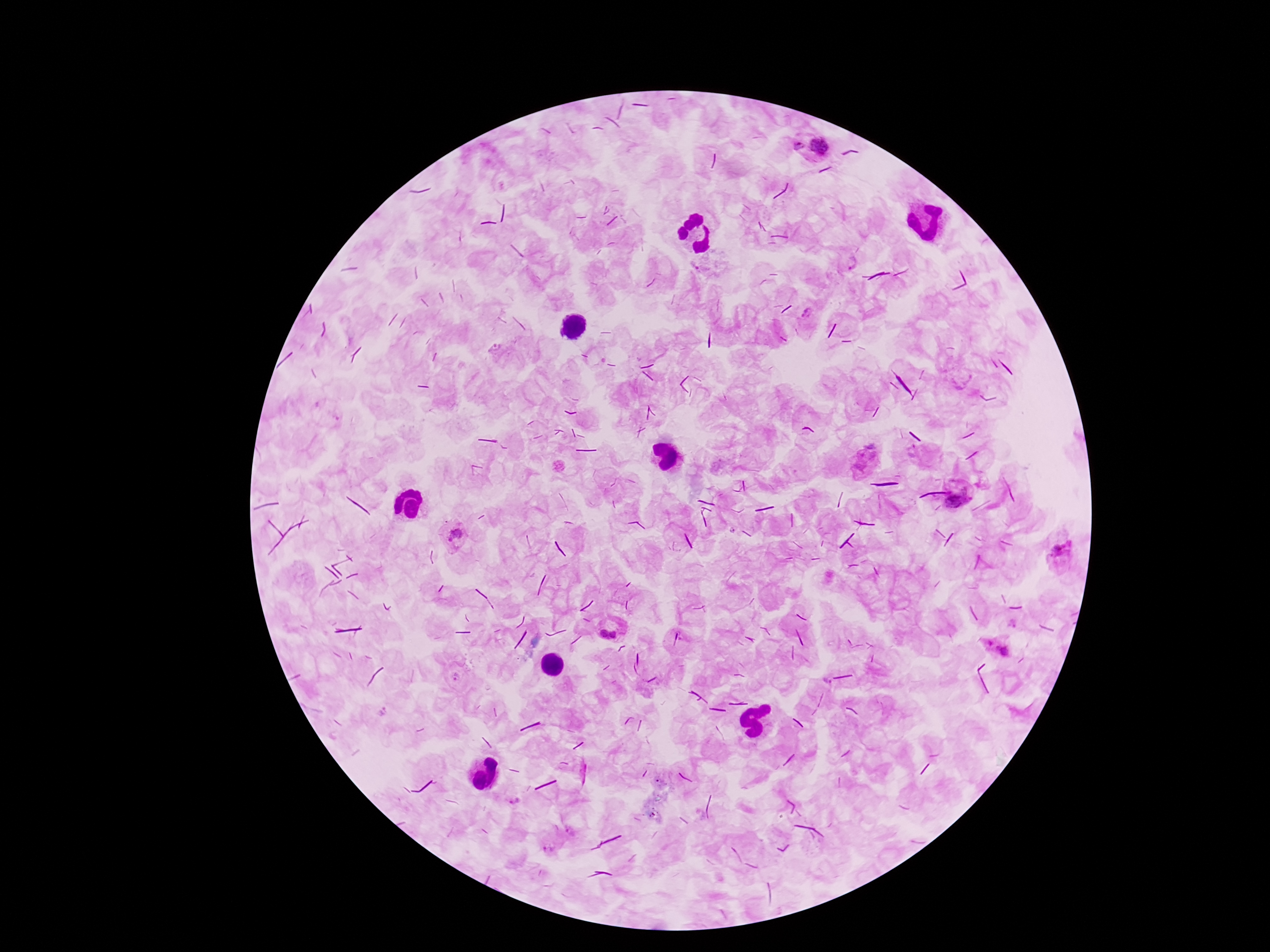
Approximate centers as (x, y) in pixels. Plasmodium parasite locations: (798, 147), (820, 147), (850, 263), (864, 459), (959, 501), (452, 535), (1065, 557), (603, 633), (614, 634), (998, 649), (455, 677), (381, 712), (515, 801), (572, 830), (548, 848). Image is 1270×952 pixels. Giemsa stain. Photographed through the microscope eyepiece with a smartphone camera. One field from this slide. 100x magnification. Patient malaria status: positive. Thick blood smear.